Identify the preparation type.
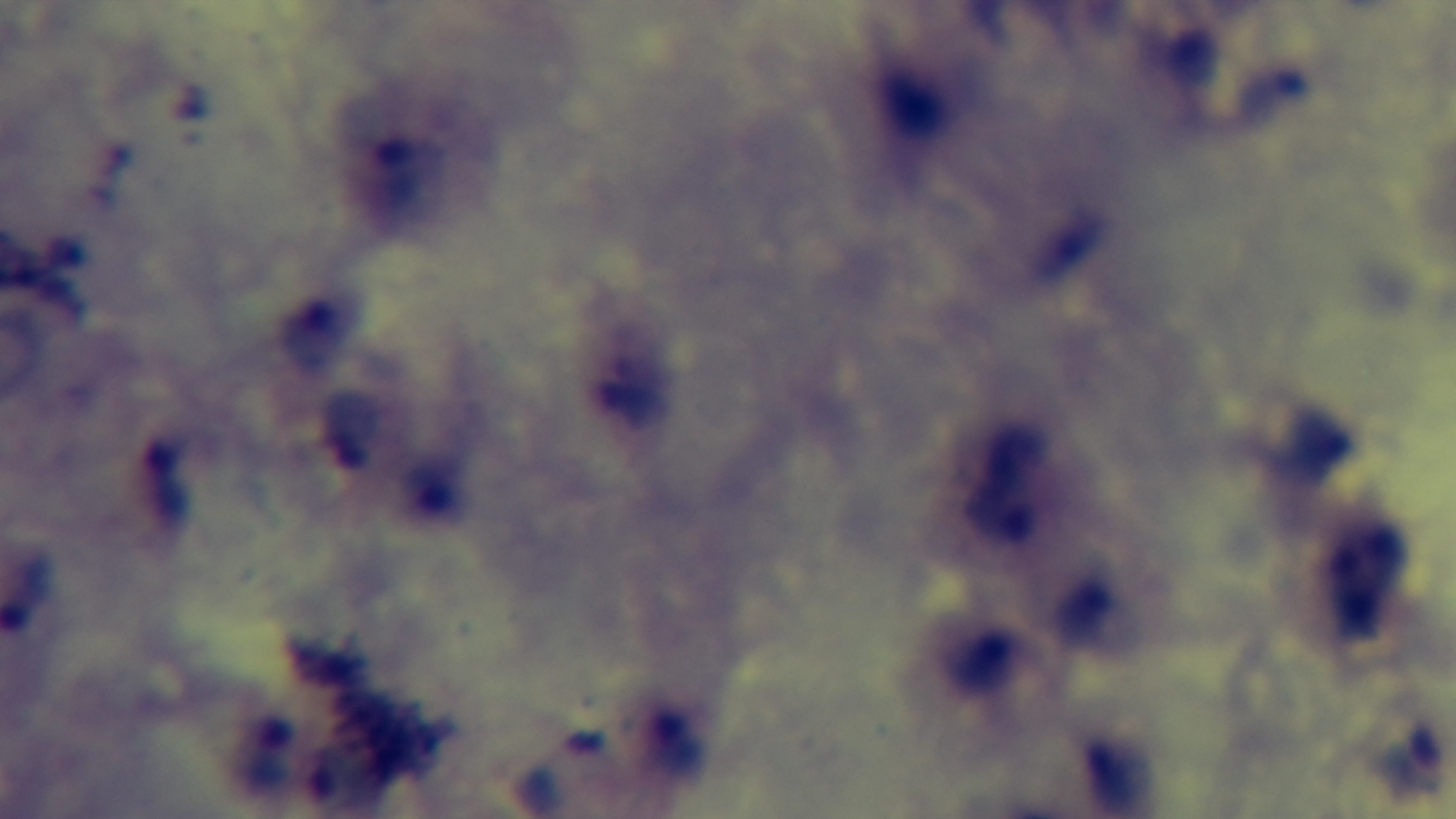

A thick smear.

Giemsa-stained. Photomicrograph. Malaria status: infected. Captured with a mounted 4K digital camera. Single field of view. Oil-immersion objective, 100x.